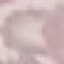
result: no malaria parasites seen
image_type: automatically extracted cell patch, resized to 64 × 64 pixels
preparation: thin blood smear
stain: Giemsa
capture: smartphone through the microscope eyepiece